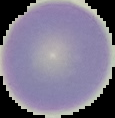

Summary:
  - Preparation: thin blood film
  - Image size: 115×118 pixels
  - Image type: segmented cell region on a black background
  - Malaria status: uninfected